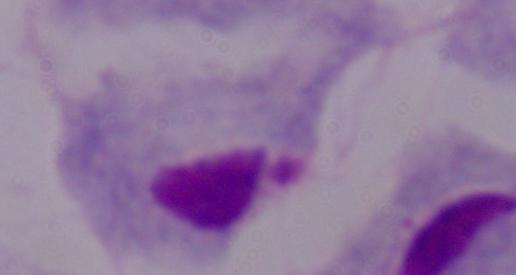
modality = micrograph
magnification = 1000x
identification = trichomonad